Locate every malaria parasite.
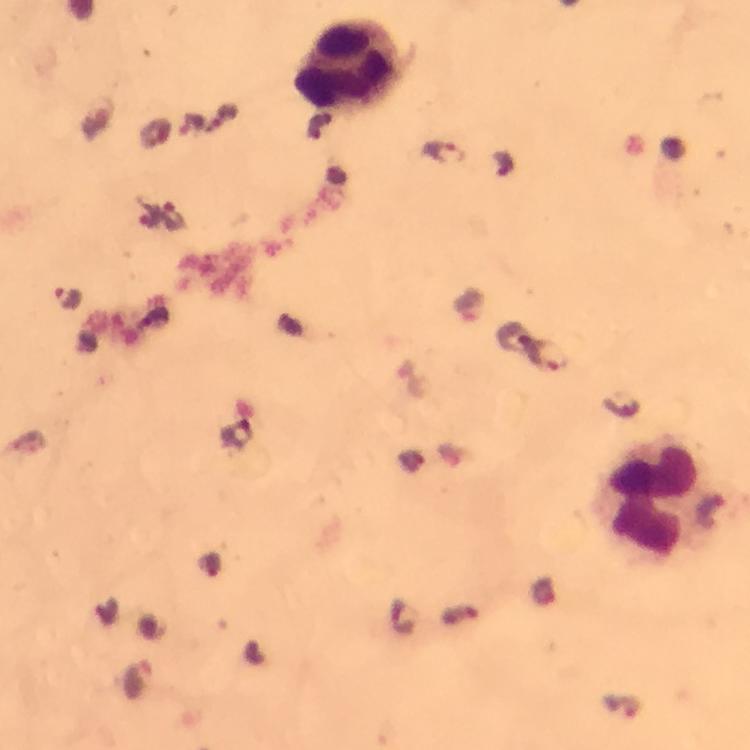

Approximate object centers, in pixels from the top-left corner.
Malaria parasites: (x=444, y=153), (x=66, y=298).

Leukocyte locations: (x=349, y=67), (x=649, y=498). Giemsa-stained preparation. 100x magnification. Photographed with a smartphone mounted on the microscope. Cropped region of a single field of view. Immersion oil applied. Image is 750×750 pixels. From a malaria diagnostic workup. Thick smear.